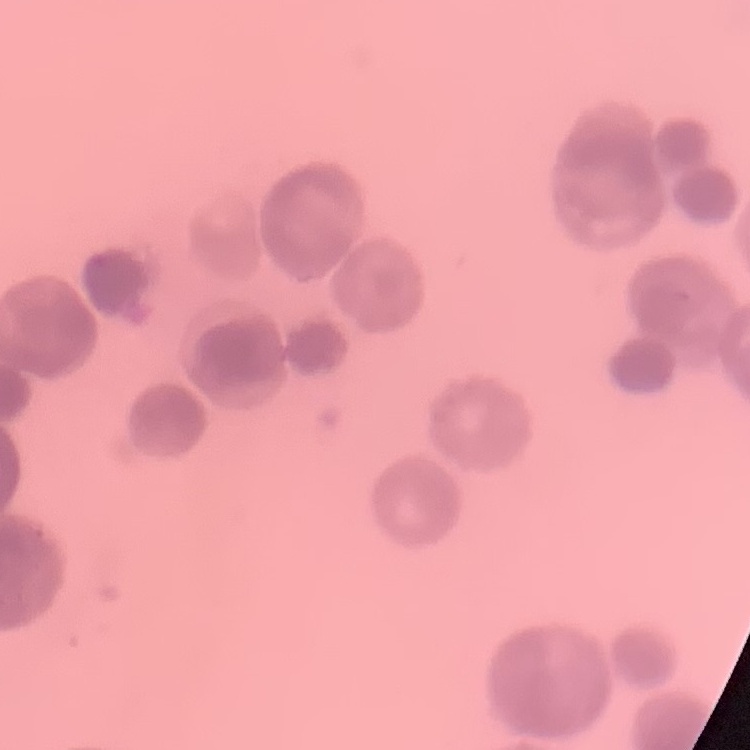

The red blood cells show rouleaux formation. Field's or Giemsa stain. One tile cut from a larger photomicrograph. Thin peripheral smear.